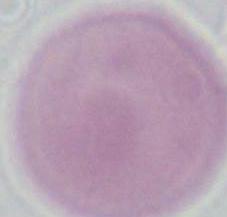

Summary:
  - Modality: photomicrograph
  - Magnification: 1000x
  - Identification: red blood cell